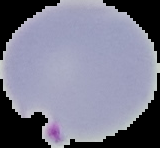
preparation = thin blood smear
image size = 160×148 pixels
result = Plasmodium parasites detected
image type = segmented cell region with the area outside set to black